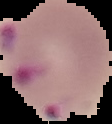
Segmented cell region on a black background. Image is 112×124 pixels. Malaria status: parasitized. From a thin blood film.